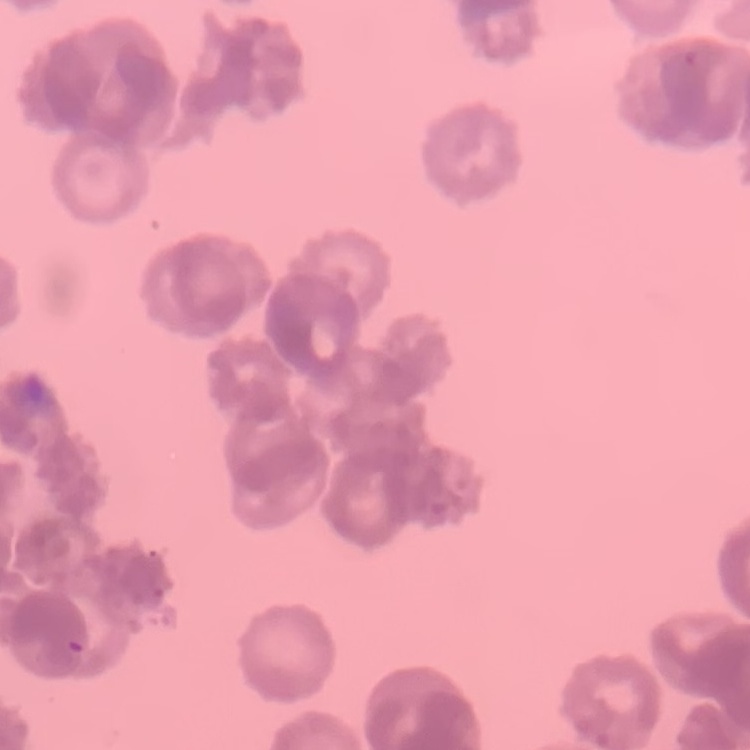
The red blood cells show rouleaux formation. Thin peripheral smear. Field's or Giemsa stain. One tile cut from a larger photomicrograph.